Classify this cell by malaria status.
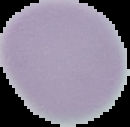
It is uninfected.

{
  "image_type": "cell region segmented out of the field of view; surrounding area masked to black",
  "preparation": "thin blood smear",
  "image_size": "130×127 pixels"
}